Comment on the morphology of the erythrocytes.
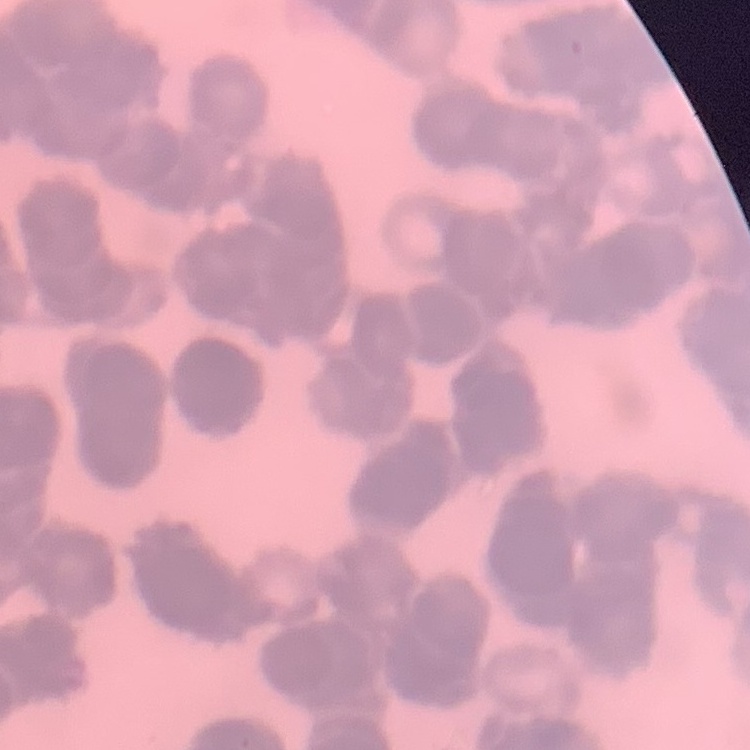

They show rouleaux formation.

{
  "preparation": "thin blood film",
  "image_type": "square crop of a larger photomicrograph",
  "stain": "Field's or Giemsa"
}